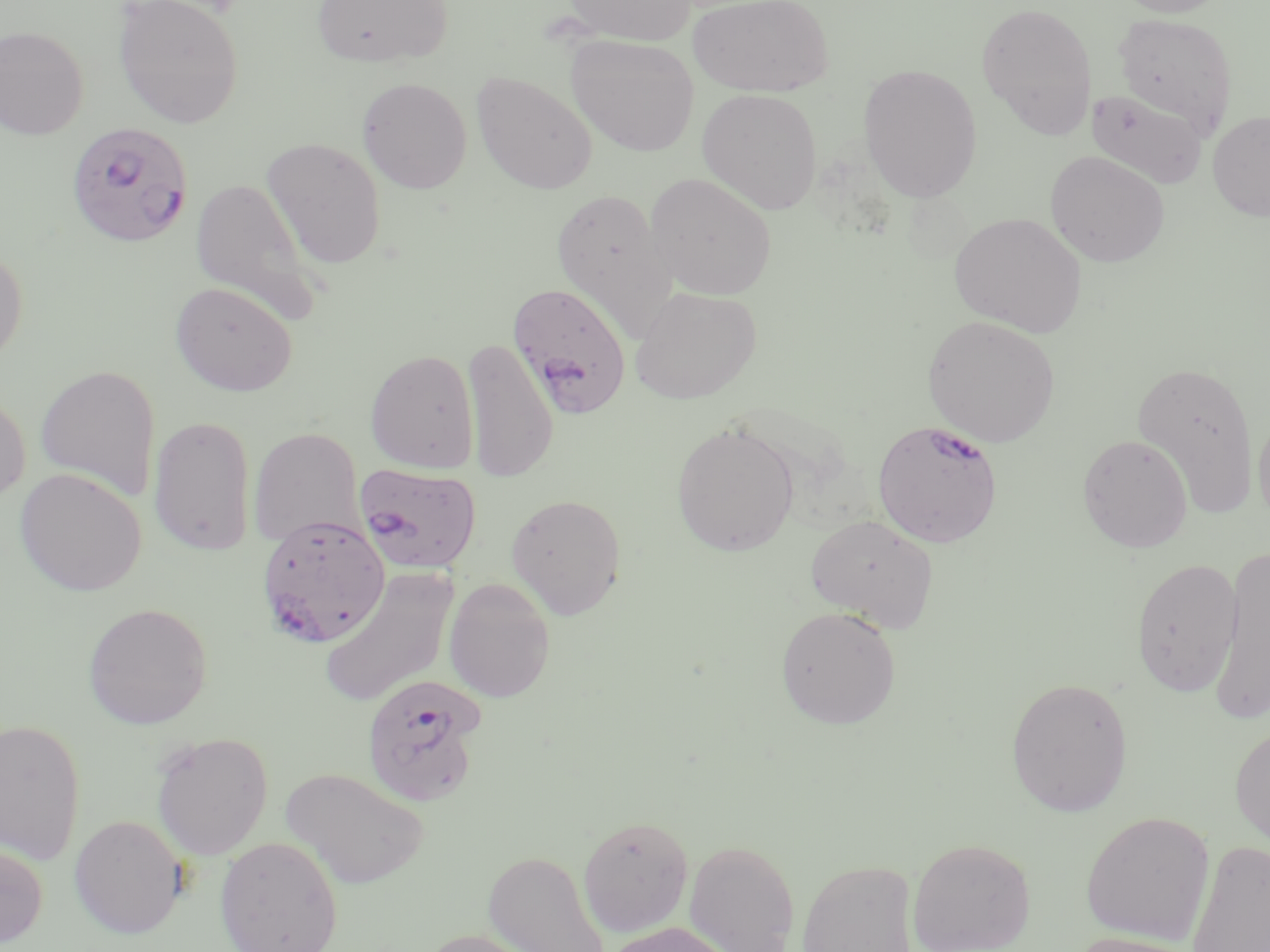
Summary:
  - Coordinate format: approximate bounding boxes as named x1/y1/x2/y2 corners in pixels
  - Plasmodium falciparum-infected red blood cell locations: (x1=65, y1=122, x2=194, y2=248), (x1=507, y1=281, x2=633, y2=419), (x1=872, y1=419, x2=1003, y2=548), (x1=355, y1=462, x2=481, y2=574), (x1=257, y1=515, x2=389, y2=647), (x1=360, y1=673, x2=486, y2=807)
  - Uninfected red blood cell locations: (x1=113, y1=0, x2=245, y2=128), (x1=311, y1=0, x2=451, y2=68), (x1=560, y1=0, x2=698, y2=45), (x1=688, y1=0, x2=833, y2=96), (x1=1115, y1=0, x2=1230, y2=17), (x1=976, y1=1, x2=1097, y2=138), (x1=1113, y1=12, x2=1238, y2=135), (x1=0, y1=25, x2=90, y2=139), (x1=566, y1=34, x2=699, y2=155), (x1=858, y1=64, x2=982, y2=202), (x1=471, y1=70, x2=598, y2=194), (x1=357, y1=77, x2=472, y2=193), (x1=697, y1=88, x2=822, y2=214), (x1=1086, y1=88, x2=1207, y2=189), (x1=1208, y1=110, x2=1270, y2=221), (x1=261, y1=137, x2=388, y2=269), (x1=1045, y1=150, x2=1169, y2=267), (x1=645, y1=173, x2=777, y2=300), (x1=191, y1=176, x2=324, y2=324), (x1=551, y1=187, x2=678, y2=338), (x1=949, y1=212, x2=1086, y2=337), (x1=0, y1=242, x2=29, y2=374), (x1=170, y1=280, x2=298, y2=397), (x1=629, y1=285, x2=762, y2=404), (x1=923, y1=315, x2=1061, y2=446), (x1=462, y1=336, x2=557, y2=484), (x1=365, y1=349, x2=480, y2=473), (x1=1131, y1=359, x2=1259, y2=516), (x1=34, y1=364, x2=161, y2=502), (x1=0, y1=388, x2=32, y2=507), (x1=1253, y1=408, x2=1270, y2=530), (x1=148, y1=414, x2=258, y2=557), (x1=672, y1=420, x2=799, y2=557), (x1=248, y1=426, x2=365, y2=550), (x1=1078, y1=434, x2=1193, y2=552), (x1=15, y1=468, x2=147, y2=596), (x1=506, y1=493, x2=627, y2=620), (x1=805, y1=513, x2=938, y2=630), (x1=1208, y1=546, x2=1270, y2=725), (x1=1130, y1=557, x2=1243, y2=697), (x1=318, y1=566, x2=460, y2=709), (x1=444, y1=577, x2=556, y2=702), (x1=82, y1=602, x2=213, y2=729), (x1=775, y1=605, x2=902, y2=729), (x1=1004, y1=676, x2=1134, y2=817), (x1=0, y1=717, x2=86, y2=864), (x1=1230, y1=723, x2=1270, y2=851), (x1=150, y1=731, x2=273, y2=860), (x1=280, y1=766, x2=430, y2=890), (x1=1080, y1=811, x2=1215, y2=945), (x1=69, y1=814, x2=189, y2=938), (x1=578, y1=815, x2=694, y2=937), (x1=215, y1=836, x2=343, y2=952), (x1=906, y1=837, x2=1037, y2=952), (x1=684, y1=839, x2=800, y2=952), (x1=1186, y1=839, x2=1270, y2=952), (x1=0, y1=840, x2=48, y2=949), (x1=483, y1=850, x2=611, y2=952), (x1=797, y1=858, x2=918, y2=952), (x1=605, y1=921, x2=735, y2=952), (x1=415, y1=928, x2=544, y2=952), (x1=1067, y1=932, x2=1204, y2=952)
  - Slide-level diagnosis: Plasmodium falciparum
  - Preparation: thin blood smear
  - Field of view: one of a larger specimen
  - Magnification: 1000x
  - Image size: 1270×952 pixels
  - Modality: optical microscopy
  - Stain: May-Grünwald-Giemsa